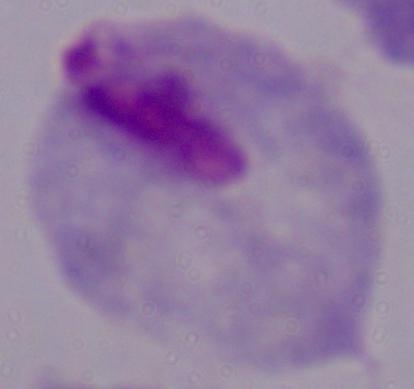 1000x magnification. Photomicrograph. A trichomonad is shown.